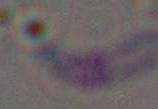
Micrograph. Toxoplasma gondii is shown. 1000x magnification.